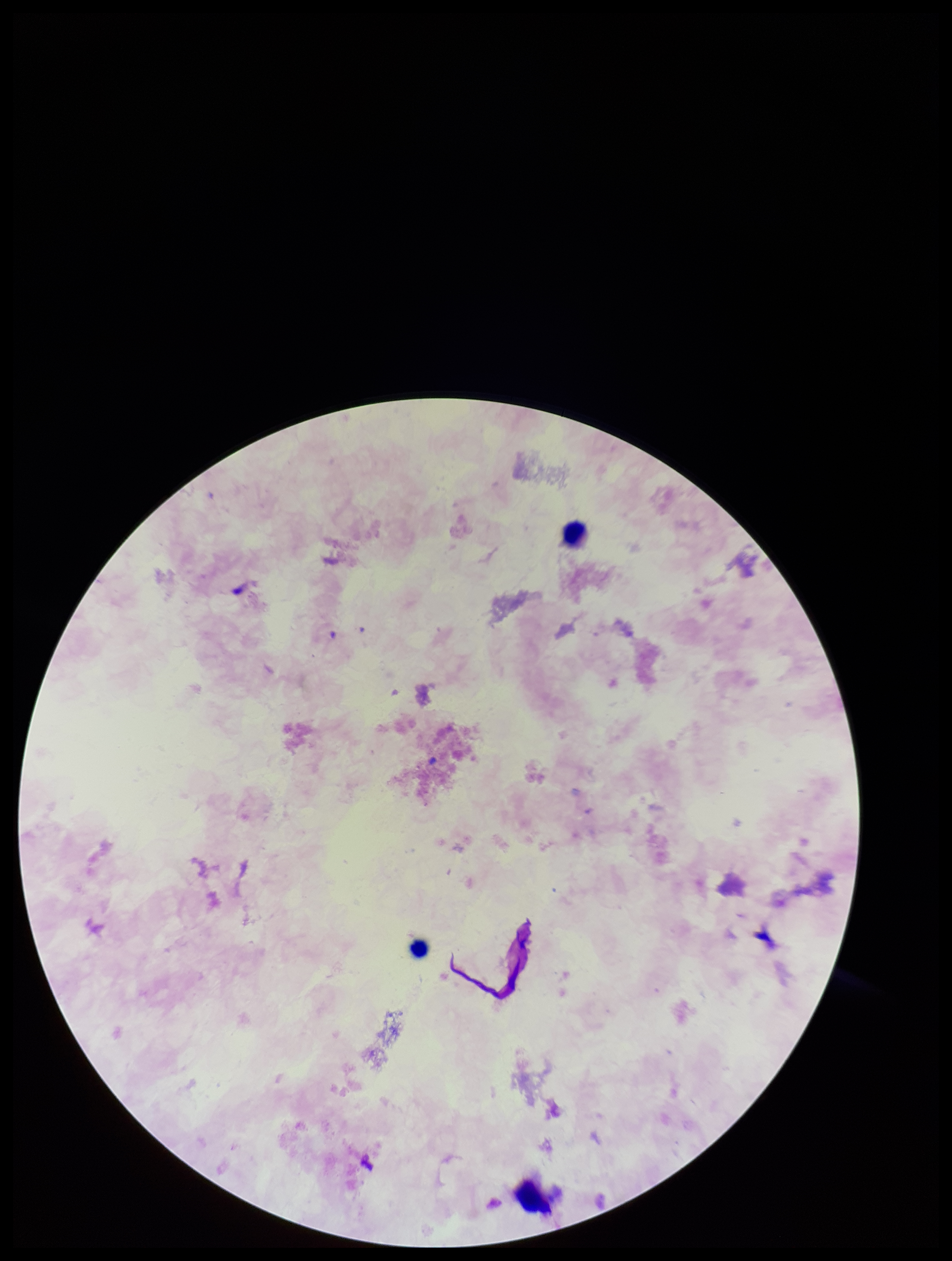

Summary:
  - Preparation: thick
  - Plasmodium parasites: none identified
  - Capture: smartphone photograph through the microscope eyepiece
  - Patient malaria status: negative
  - Leukocyte count: 3
  - Parasite count: 0
  - Image size: 952×1261 pixels
  - Stain: Giemsa
  - Field of view: single